Assess this cell for malaria.
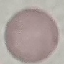
It is uninfected.

Summary:
  - Image type: automatically extracted cell patch, resized to 64 × 64 pixels
  - Capture: smartphone through the microscope eyepiece
  - Preparation: thin blood smear
  - Stain: Giemsa